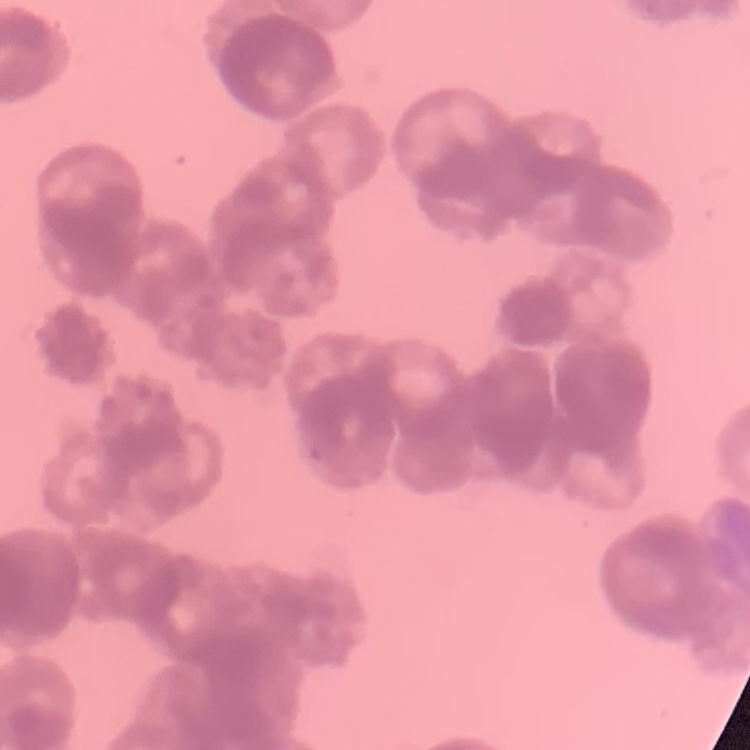

red_blood_cell_morphology: rouleaux formation
preparation: thin peripheral smear
image_type: square crop of a larger photomicrograph
stain: Field's or Giemsa